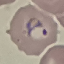
malaria status = parasitized
image type = automatically extracted cell patch, resized to 64 × 64 pixels
stain = Giemsa
capture = smartphone camera at the microscope eyepiece
preparation = thin blood film